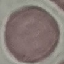 Result: no malaria parasites detected. Giemsa stain. Thin blood film. Automatically extracted cell patch, resized to 64 × 64 pixels. Acquired by smartphone through the microscope eyepiece.